State the blood parasite species.
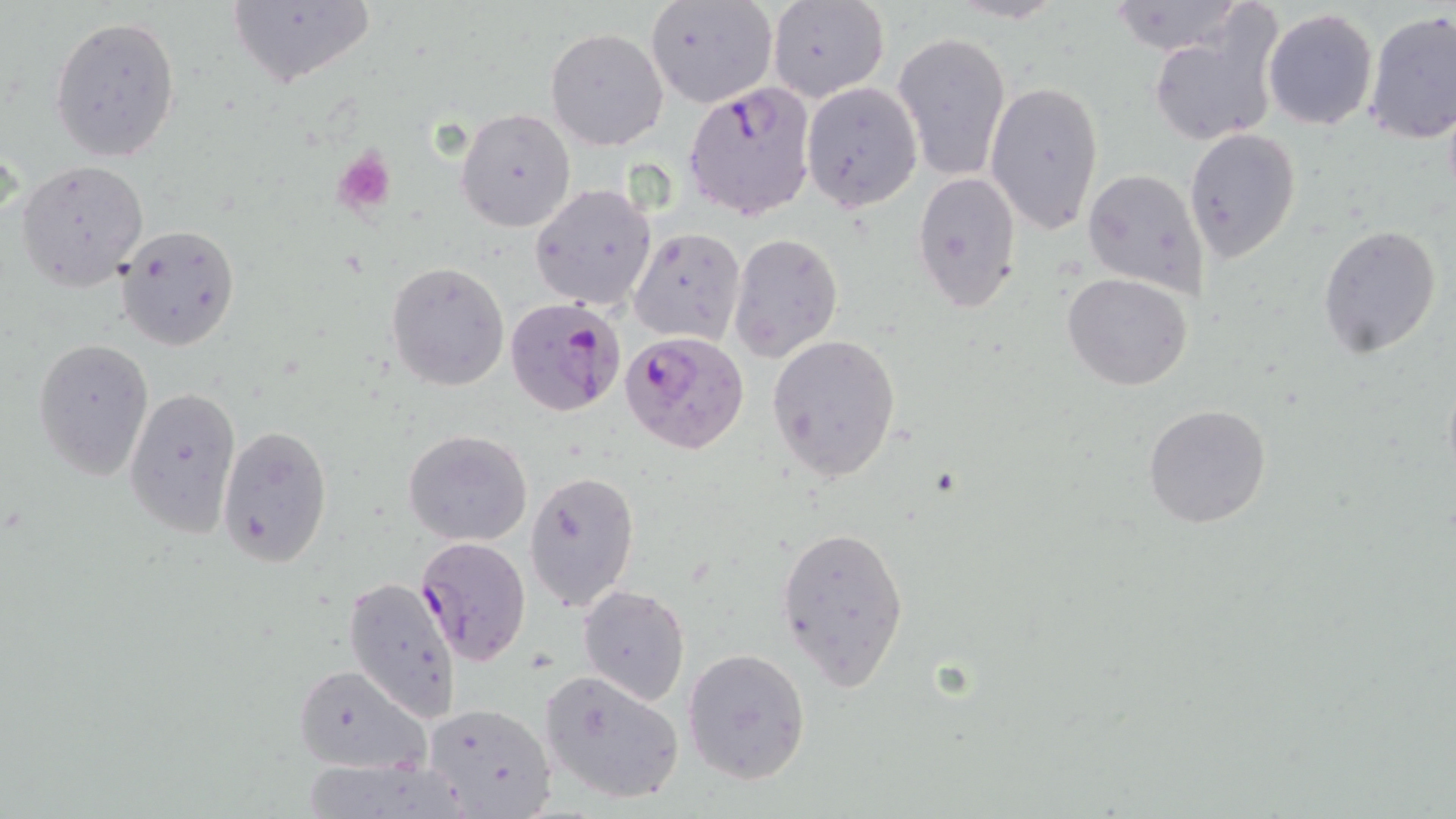

Plasmodium falciparum.

Approximate bounding boxes as (x1, y1, x2, y2) in pixels. Uninfected red blood cell locations: (646, 0, 779, 109), (1107, 0, 1247, 56), (226, 1, 378, 90), (767, 1, 889, 102), (946, 1, 1068, 24), (1262, 8, 1378, 131), (1363, 10, 1456, 144), (1149, 14, 1283, 149), (51, 15, 181, 163), (546, 28, 668, 150), (893, 31, 1012, 182), (800, 80, 921, 212), (984, 80, 1105, 235), (455, 107, 577, 232), (1184, 128, 1302, 261), (17, 161, 149, 290), (1082, 168, 1210, 297), (912, 170, 1021, 313), (530, 182, 656, 312), (115, 224, 240, 352), (1317, 224, 1442, 361), (629, 226, 746, 346), (729, 234, 843, 361), (386, 261, 509, 390), (1062, 273, 1195, 392), (767, 333, 901, 484), (33, 338, 154, 479), (124, 384, 242, 539), (1142, 404, 1272, 530), (217, 426, 332, 567), (403, 430, 534, 546), (524, 469, 640, 612), (776, 522, 911, 691), (343, 577, 464, 724), (578, 585, 689, 706), (683, 648, 810, 785), (293, 663, 432, 777), (535, 668, 686, 806), (423, 702, 558, 816). Plasmodium falciparum-infected red blood cell locations: (684, 80, 816, 222), (505, 297, 624, 418), (619, 328, 749, 452), (416, 536, 531, 665). Platelet locations: (332, 147, 397, 214). Light microscopy. May-Grünwald-Giemsa stain. Image is 1456×819 pixels. One field of a larger specimen. 1000x magnification. Thin blood smear.